Report the malaria status of this cell.
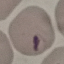
Parasitized.

Summary:
  - Capture: smartphone camera at the microscope eyepiece
  - Stain: Giemsa
  - Preparation: thin blood film
  - Image type: automatically extracted cell patch, resized to 64 × 64 pixels